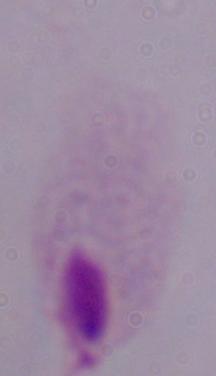
magnification = 1000x
identification = trichomonad
modality = photomicrograph